State the preparation type.
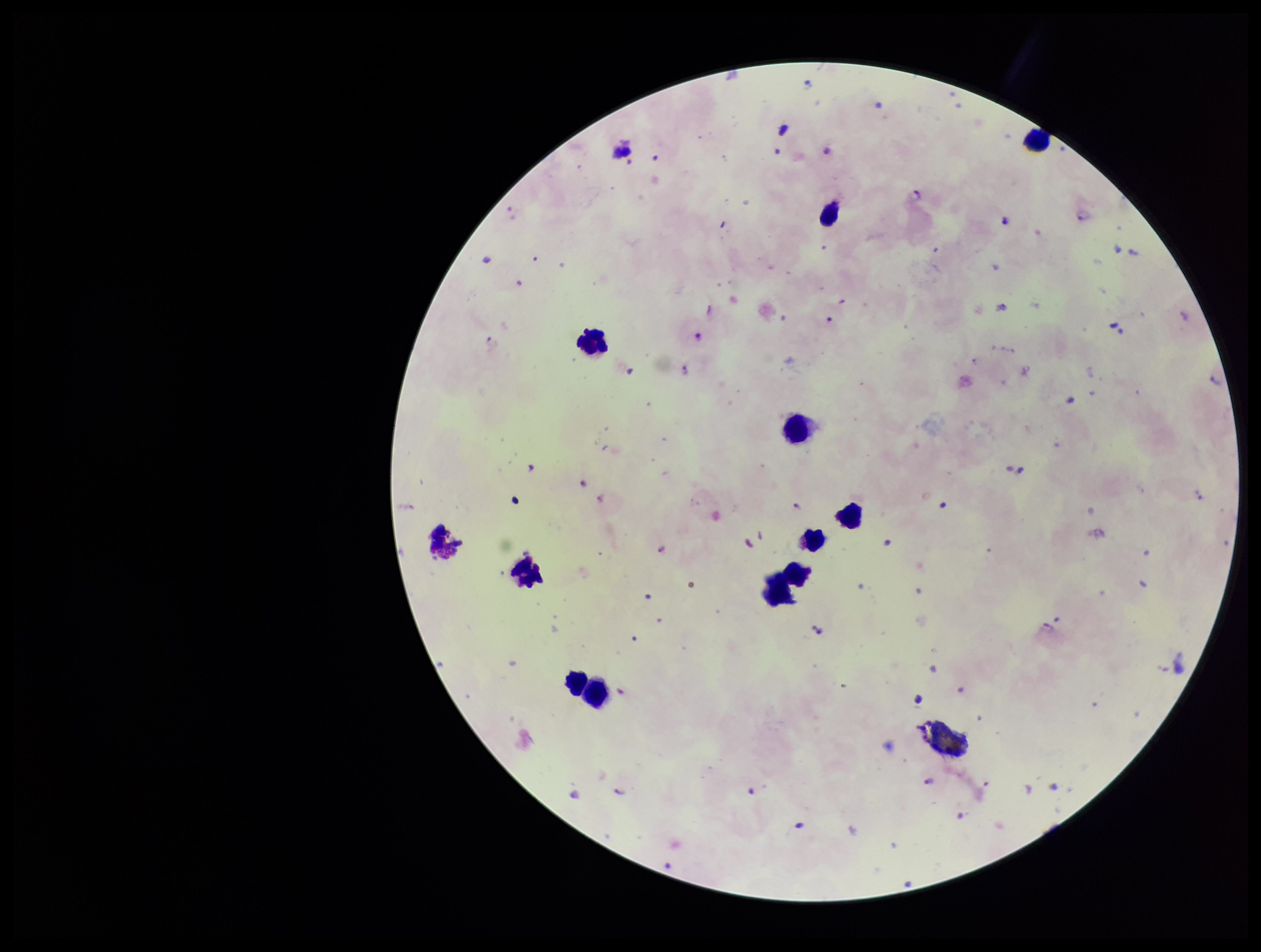
It is a thick blood smear.

leukocyte count = 10
patient malaria status = positive
stain = Giemsa
image size = 1261×952 pixels
species reported for this patient = Plasmodium falciparum
capture = smartphone photograph through the microscope eyepiece
Plasmodium parasites = identified
field of view = single
parasite count = 19